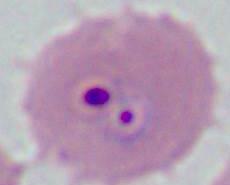
modality = micrograph
identification = Plasmodium
magnification = 400x or 1000x